Assess this cell for malaria.
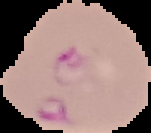
Parasitized.

Summary:
  - Preparation: thin blood film
  - Image size: 151×133 pixels
  - Image type: segmented cell region with the area outside set to black